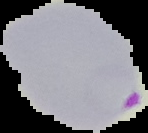

From a thin blood film. The area outside the segmented cell region is set to black. Result: Plasmodium parasites detected. Image is 148×133 pixels.